Report the malaria status of this cell.
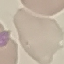

It is uninfected.

image type = automatically extracted cell patch, resized to 64 × 64 pixels
stain = Giemsa
capture = smartphone camera at the microscope eyepiece
preparation = thin smear